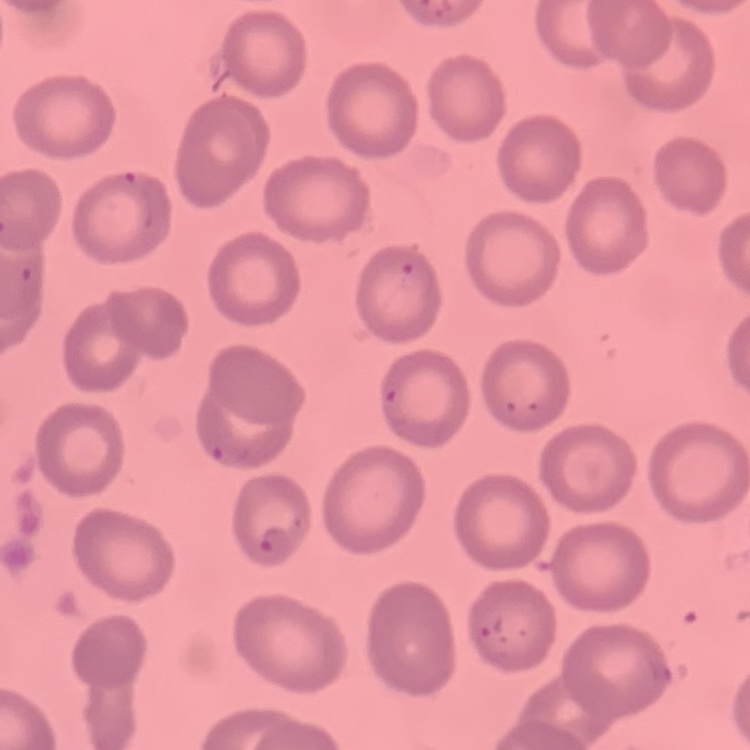
{
  "erythrocyte_morphology": "no rouleaux formation",
  "preparation": "thin peripheral smear",
  "image_type": "one tile cut from a larger photomicrograph",
  "stain": "Field's or Giemsa"
}